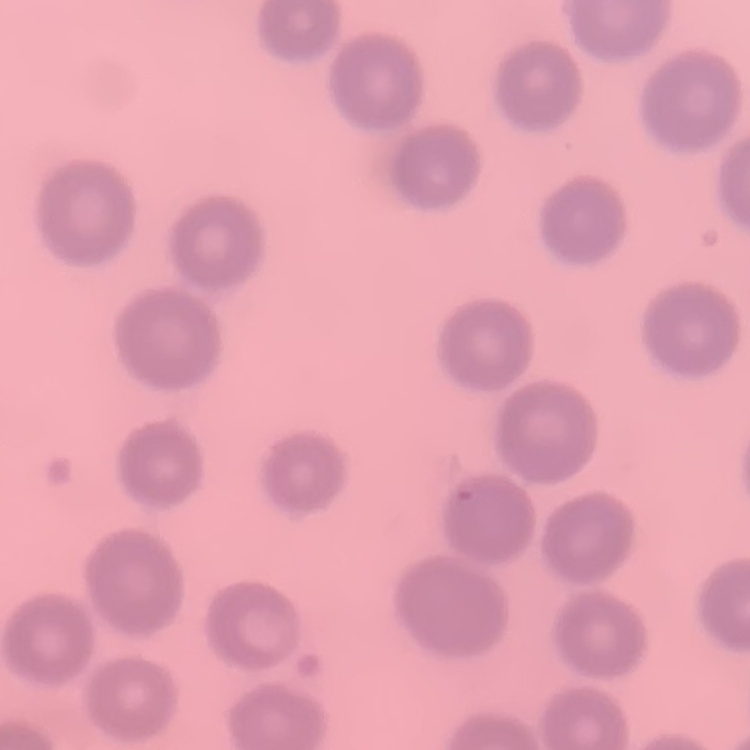 The red blood cells exhibit no rouleaux formation. Field's or Giemsa stain. Thin blood film. One tile cut from a larger photomicrograph.